Classify this cell by malaria status.
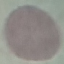
It is uninfected.

Summary:
  - Stain: Giemsa
  - Image type: cell patch, automatically extracted from a larger field of view and resized to 64 × 64 pixels
  - Preparation: thin smear
  - Capture: smartphone through the microscope eyepiece